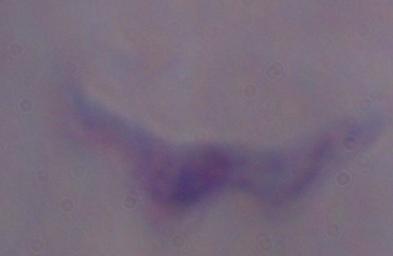
1000x magnification. A trypanosome is seen. Micrograph.